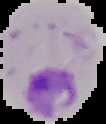
preparation = thin blood film
image size = 106×124 pixels
malaria status = parasitized
image type = segmented cell region on a black background